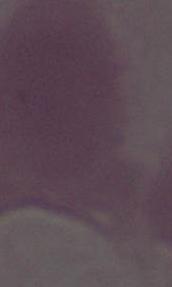

{
  "modality": "micrograph",
  "magnification": "1000x",
  "identification": "erythrocyte"
}